State the blood parasite species.
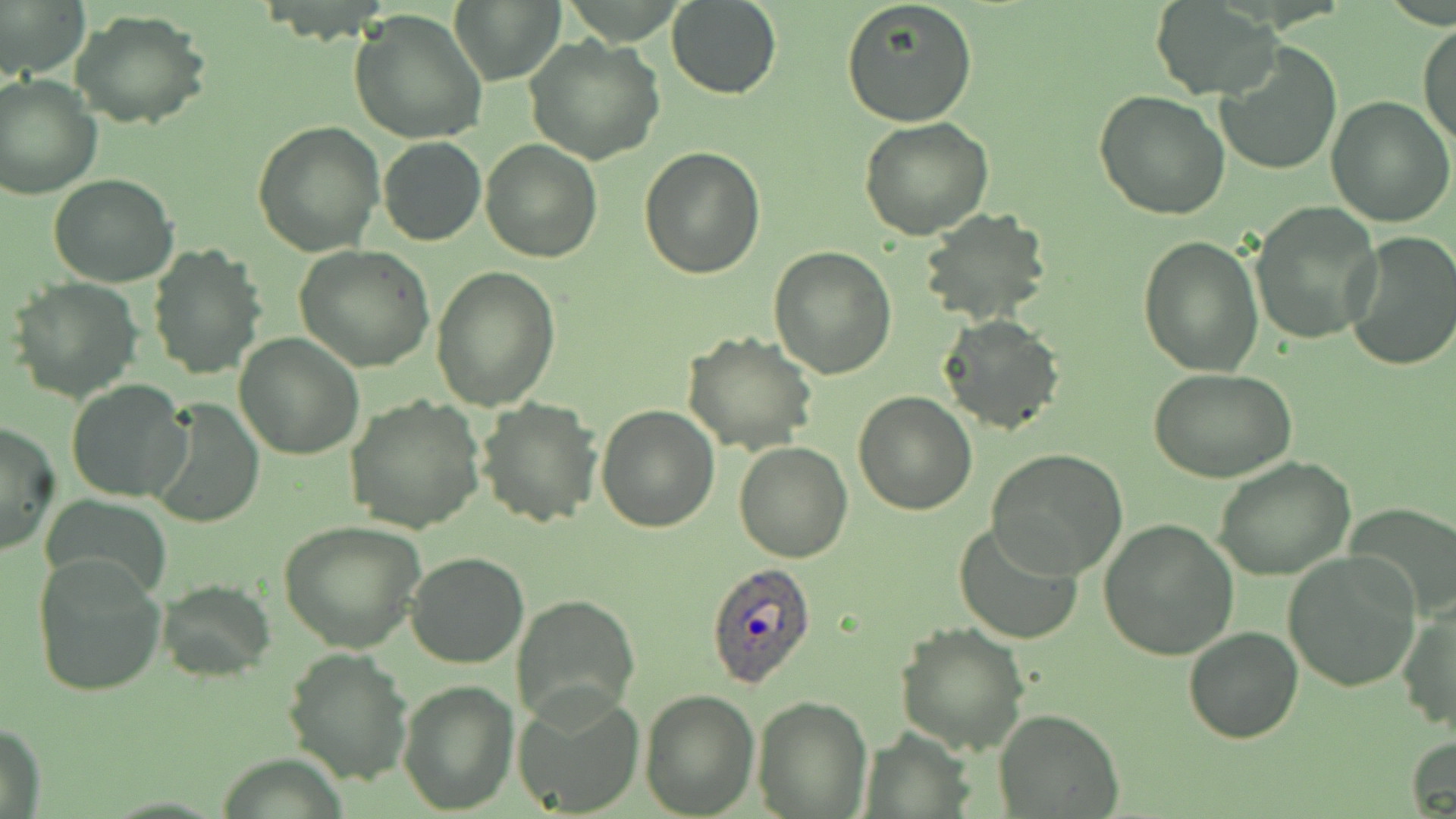
Plasmodium ovale.

Approximate bounding boxes as named x1/y1/x2/y2 corners in pixels. Plasmodium ovale-infected red blood cell locations: (x1=705, y1=562, x2=817, y2=689). Uninfected red blood cell locations: (x1=0, y1=0, x2=89, y2=77), (x1=666, y1=0, x2=781, y2=100), (x1=840, y1=0, x2=979, y2=127), (x1=450, y1=1, x2=564, y2=85), (x1=1152, y1=3, x2=1280, y2=100), (x1=70, y1=9, x2=212, y2=128), (x1=349, y1=9, x2=488, y2=145), (x1=1418, y1=23, x2=1456, y2=150), (x1=524, y1=36, x2=665, y2=165), (x1=1214, y1=40, x2=1343, y2=176), (x1=0, y1=74, x2=101, y2=199), (x1=1094, y1=90, x2=1230, y2=222), (x1=1327, y1=96, x2=1456, y2=227), (x1=251, y1=118, x2=384, y2=257), (x1=859, y1=118, x2=994, y2=241), (x1=377, y1=136, x2=486, y2=246), (x1=480, y1=139, x2=601, y2=262), (x1=639, y1=148, x2=766, y2=280), (x1=48, y1=173, x2=181, y2=288), (x1=1250, y1=202, x2=1382, y2=344), (x1=916, y1=209, x2=1053, y2=328), (x1=1344, y1=232, x2=1456, y2=371), (x1=1137, y1=235, x2=1264, y2=377), (x1=147, y1=245, x2=265, y2=379), (x1=294, y1=246, x2=435, y2=373), (x1=767, y1=246, x2=896, y2=378), (x1=432, y1=266, x2=561, y2=411), (x1=7, y1=277, x2=144, y2=404), (x1=939, y1=313, x2=1065, y2=436), (x1=682, y1=331, x2=820, y2=456), (x1=234, y1=333, x2=365, y2=460), (x1=1147, y1=366, x2=1298, y2=484), (x1=66, y1=378, x2=191, y2=502), (x1=852, y1=391, x2=978, y2=514), (x1=345, y1=395, x2=486, y2=534), (x1=149, y1=396, x2=264, y2=528), (x1=475, y1=398, x2=603, y2=527), (x1=596, y1=405, x2=721, y2=532), (x1=0, y1=420, x2=60, y2=558), (x1=734, y1=442, x2=853, y2=563), (x1=987, y1=449, x2=1128, y2=579), (x1=1212, y1=456, x2=1356, y2=581), (x1=41, y1=490, x2=172, y2=600), (x1=1347, y1=508, x2=1455, y2=623), (x1=278, y1=518, x2=427, y2=653), (x1=1098, y1=518, x2=1239, y2=662), (x1=953, y1=520, x2=1083, y2=646), (x1=405, y1=551, x2=529, y2=669), (x1=1282, y1=552, x2=1422, y2=691), (x1=31, y1=553, x2=167, y2=699), (x1=154, y1=580, x2=275, y2=679), (x1=512, y1=593, x2=640, y2=723), (x1=1396, y1=601, x2=1456, y2=739), (x1=896, y1=623, x2=1029, y2=754), (x1=1183, y1=627, x2=1303, y2=743), (x1=284, y1=646, x2=410, y2=784), (x1=398, y1=679, x2=520, y2=814), (x1=638, y1=686, x2=759, y2=817), (x1=511, y1=689, x2=644, y2=818), (x1=752, y1=695, x2=872, y2=817), (x1=994, y1=708, x2=1124, y2=817), (x1=1, y1=722, x2=47, y2=819), (x1=1406, y1=736, x2=1456, y2=818). Image is 1456×819 pixels. Captured at 1000x magnification. Single field of view. May-Grünwald-Giemsa stain. Thin blood film. Light microscopy.